State the preparation type.
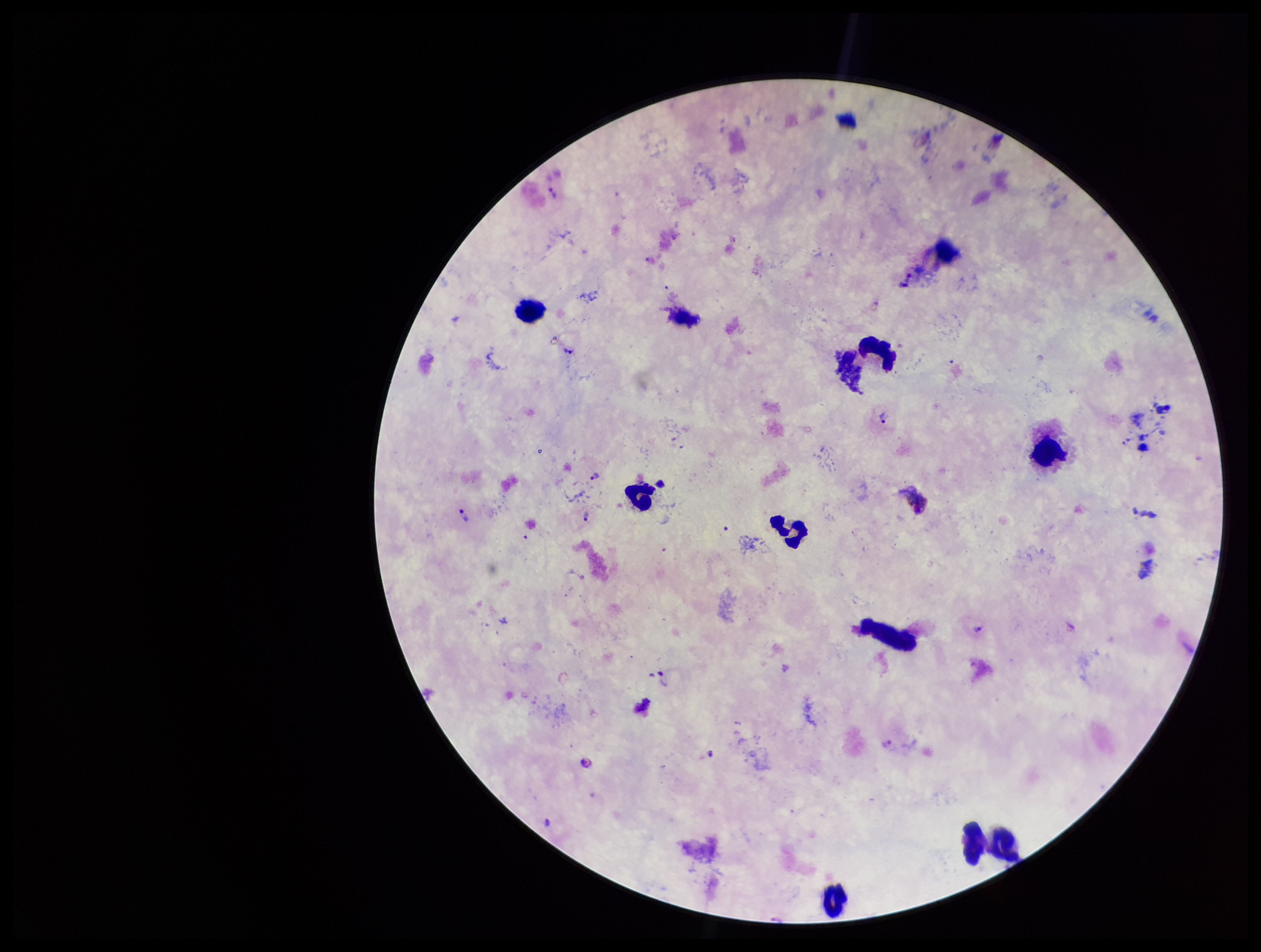

Thick.

parasite count = 10
species reported for this patient = Plasmodium vivax
Plasmodium parasites = seen
stain = Giemsa
leukocyte count = 8
capture = smartphone photograph through the microscope eyepiece
patient malaria status = positive
image size = 1261×952 pixels
field of view = single